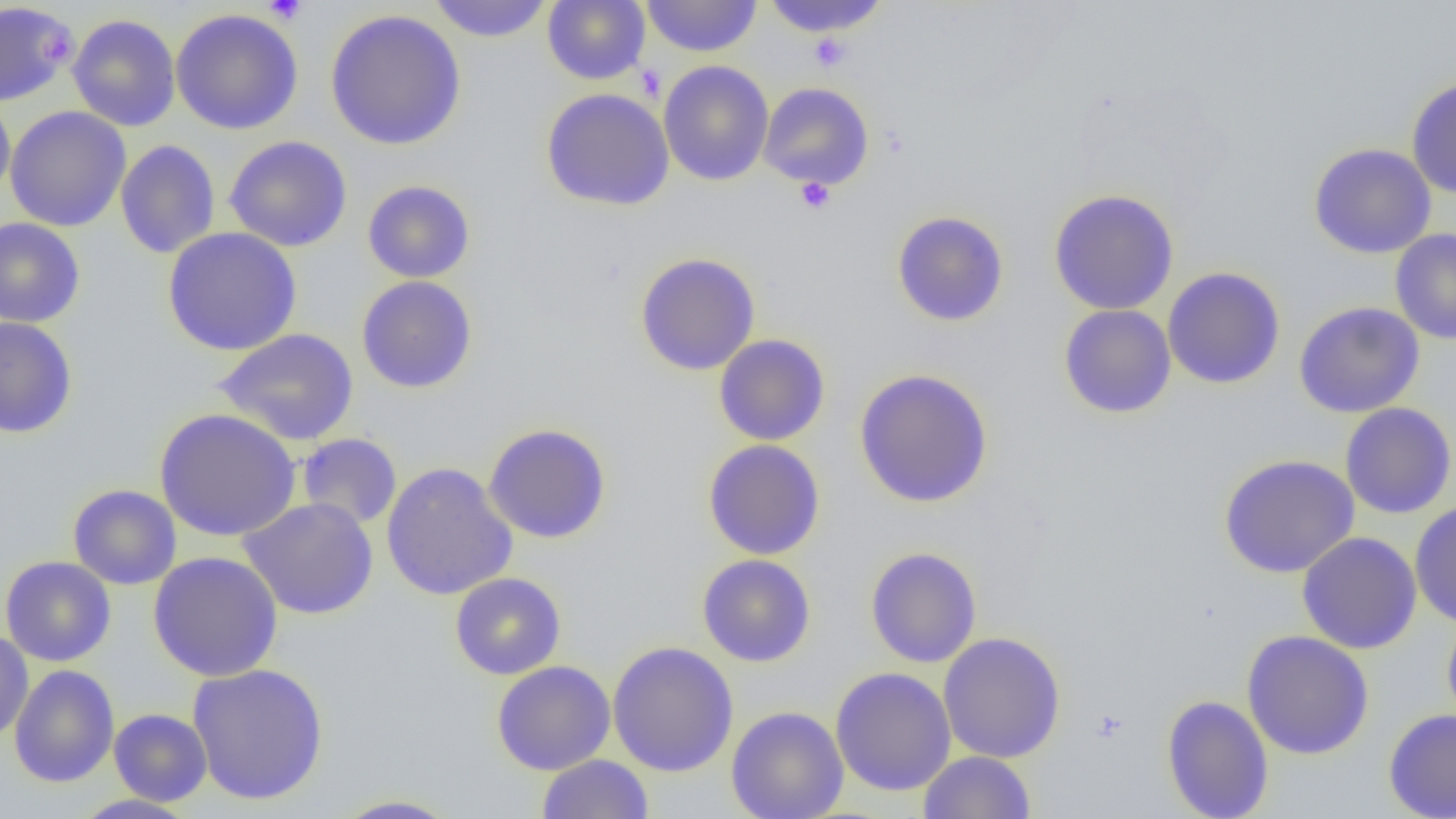
slide_level_diagnosis: negative for blood parasites
preparation: thin blood film
uninfected_red_blood_cell_locations: 'approximate bounding boxes as (x1, y1, x2, y2) in pixels: (427, 0, 554, 42), (543, 0, 650, 85), (641, 0, 762, 57), (762, 0, 889, 37), (0, 2, 75, 106), (170, 9, 304, 135), (324, 9, 467, 150), (67, 13, 181, 131), (658, 61, 774, 186), (1406, 76, 1456, 199), (758, 82, 874, 190), (541, 88, 675, 211), (0, 94, 15, 201), (4, 106, 131, 232), (224, 135, 353, 252), (115, 140, 220, 259), (1308, 142, 1437, 259), (362, 180, 475, 283), (1048, 188, 1179, 315), (891, 211, 1009, 327), (0, 217, 85, 328), (162, 227, 302, 356), (1390, 228, 1456, 344), (635, 252, 761, 376), (1163, 267, 1285, 389), (356, 275, 477, 393), (1295, 301, 1425, 418), (1059, 304, 1177, 419), (0, 317, 78, 438), (213, 328, 359, 446), (713, 334, 830, 446), (854, 368, 994, 508), (1340, 402, 1456, 519), (154, 408, 301, 541), (483, 423, 613, 544), (296, 432, 403, 530), (703, 439, 826, 560), (1219, 454, 1359, 578), (381, 461, 519, 601), (68, 484, 181, 590), (237, 497, 379, 619), (1409, 501, 1456, 628), (1297, 532, 1422, 654), (865, 547, 983, 668), (148, 551, 283, 682), (697, 554, 816, 667), (0, 556, 116, 666), (450, 572, 566, 679), (1442, 613, 1456, 733), (0, 630, 34, 743), (1242, 630, 1374, 759), (938, 631, 1067, 763), (607, 640, 739, 777), (491, 661, 616, 775), (187, 662, 329, 805), (9, 664, 120, 788), (830, 667, 957, 796), (1161, 694, 1274, 819), (725, 706, 849, 819), (108, 708, 212, 806), (1383, 708, 1456, 819), (919, 750, 1036, 819), (537, 754, 654, 819), (70, 794, 198, 818), (329, 794, 464, 818)'
image_size: 1456×819 pixels
platelet_locations: 'approximate bounding boxes as (x1, y1, x2, y2) in pixels: (261, 0, 309, 24), (0, 3, 78, 100), (37, 29, 77, 69), (809, 33, 851, 71), (795, 178, 835, 214)'
modality: optical microscopy
field_of_view: one of a larger specimen
magnification: 1000x